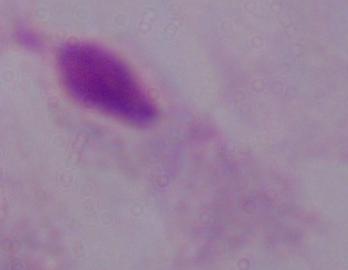
Captured at 1000x magnification. A trichomonad is shown. Micrograph.